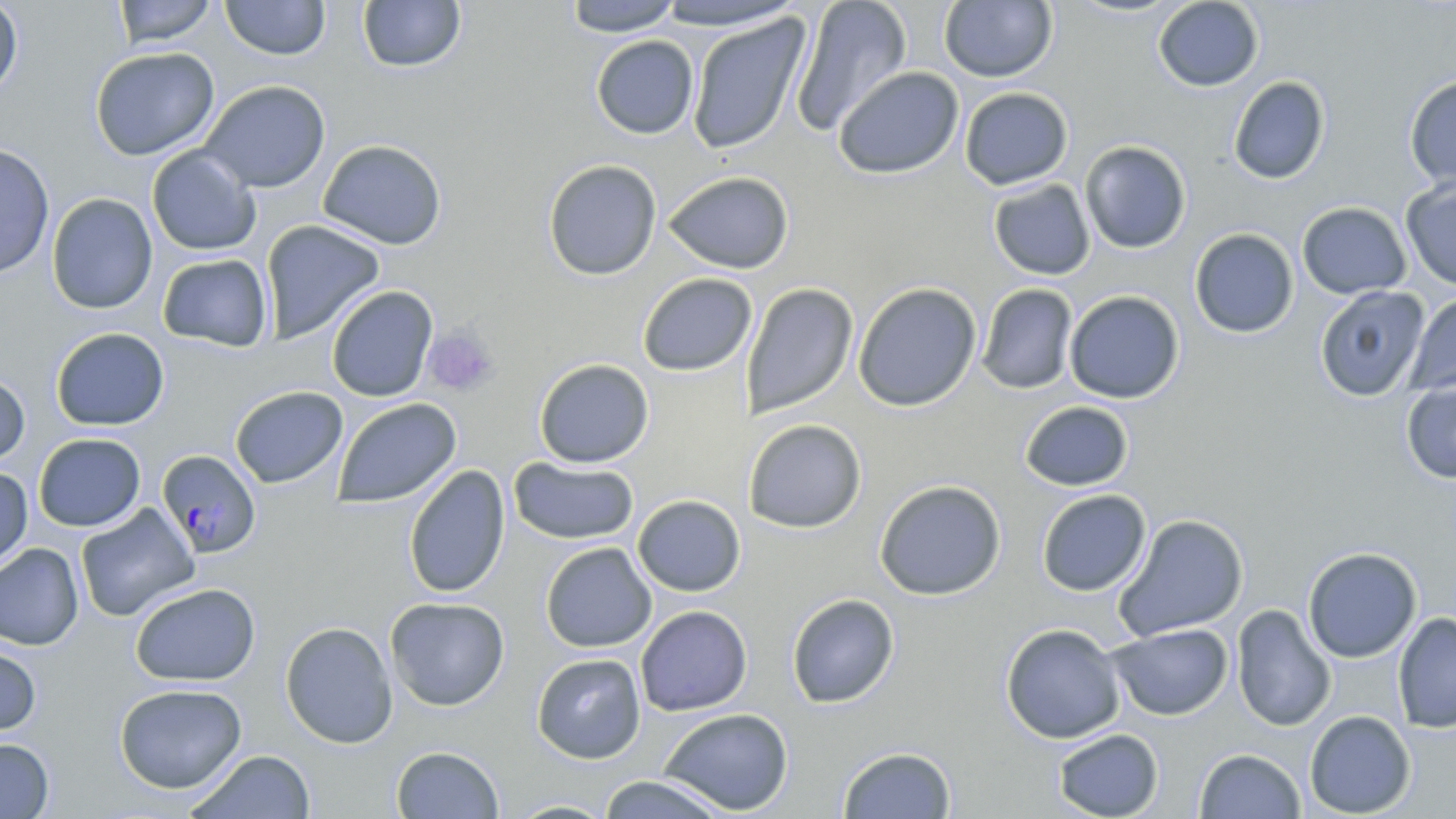

{
  "slide_level_diagnosis": "Plasmodium falciparum",
  "platelet_locations": "approximate bounding boxes as [x1, y1, x2, y2] in pixels: [422, 325, 500, 396]",
  "modality": "optical microscopy",
  "field_of_view": "single",
  "magnification": "1000x",
  "stain": "May-Grünwald-Giemsa",
  "preparation": "thin blood film",
  "plasmodium_falciparum_infected_red_blood_cell_locations": "approximate bounding boxes as [x1, y1, x2, y2] in pixels: [157, 450, 262, 558]",
  "uninfected_red_blood_cell_locations": "approximate bounding boxes as [x1, y1, x2, y2] in pixels: [0, 0, 23, 101], [113, 0, 217, 48], [220, 0, 331, 60], [357, 0, 466, 74], [564, 0, 683, 36], [790, 0, 913, 136], [1152, 0, 1264, 92], [652, 1, 807, 32], [939, 1, 1058, 83], [686, 14, 811, 154], [590, 35, 699, 139], [89, 46, 220, 161], [833, 66, 964, 179], [1403, 74, 1456, 191], [1227, 76, 1330, 185], [199, 80, 331, 193], [959, 87, 1073, 190], [317, 139, 447, 250], [1079, 140, 1192, 254], [0, 142, 55, 279], [147, 146, 261, 255], [542, 159, 662, 280], [663, 171, 794, 274], [1400, 176, 1456, 290], [984, 178, 1085, 391], [987, 178, 1095, 280], [46, 192, 158, 315], [1297, 201, 1412, 300], [260, 219, 386, 343], [1189, 228, 1299, 338], [157, 254, 273, 352], [637, 272, 757, 377], [852, 281, 982, 412], [740, 283, 859, 419], [976, 284, 1079, 395], [325, 285, 438, 402], [1313, 285, 1430, 402], [1064, 290, 1185, 404], [1405, 292, 1456, 394], [50, 327, 169, 431], [534, 358, 654, 468], [0, 371, 30, 466], [1401, 379, 1456, 483], [229, 385, 348, 488], [332, 397, 462, 509], [1019, 400, 1134, 492], [743, 418, 867, 534], [33, 433, 146, 531], [509, 456, 639, 545], [403, 465, 511, 598], [0, 466, 33, 570], [874, 479, 1006, 600], [1036, 489, 1151, 597], [632, 494, 746, 596], [76, 503, 200, 622], [1113, 513, 1249, 641], [540, 542, 656, 653], [0, 543, 84, 650], [1302, 547, 1422, 663], [129, 582, 261, 687], [786, 593, 900, 709], [385, 597, 510, 711], [1231, 604, 1336, 731], [635, 605, 753, 716], [1392, 611, 1456, 734], [279, 621, 398, 748], [1000, 623, 1126, 744], [1107, 623, 1233, 721], [0, 644, 42, 737], [532, 652, 646, 764], [114, 683, 247, 794], [658, 708, 794, 816], [1304, 710, 1416, 817], [1052, 728, 1164, 818], [0, 738, 54, 818], [390, 745, 504, 818], [837, 745, 957, 819], [1195, 748, 1306, 818], [186, 750, 316, 818], [597, 774, 731, 819], [503, 799, 618, 818]",
  "image_size": "1456×819 pixels"
}